Classify this cell by malaria status.
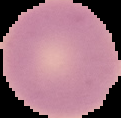
Uninfected.

{
  "image_type": "cell region segmented out of the field of view; surrounding area masked to black",
  "image_size": "121×118 pixels",
  "preparation": "thin blood film"
}